Identify the parasite.
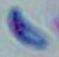
This is Toxoplasma gondii.

Photomicrograph. Captured at 1000x magnification.